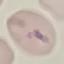
result = malaria parasites identified
capture = smartphone through the microscope eyepiece
preparation = thin blood smear
stain = Giemsa
image type = automatically extracted cell patch, resized to 64 × 64 pixels